Report the malaria status of this cell.
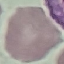
Uninfected.

{
  "capture": "smartphone camera at the microscope eyepiece",
  "stain": "Giemsa",
  "image_type": "automatically extracted cell patch, resized to 64 × 64 pixels",
  "preparation": "thin blood film"
}